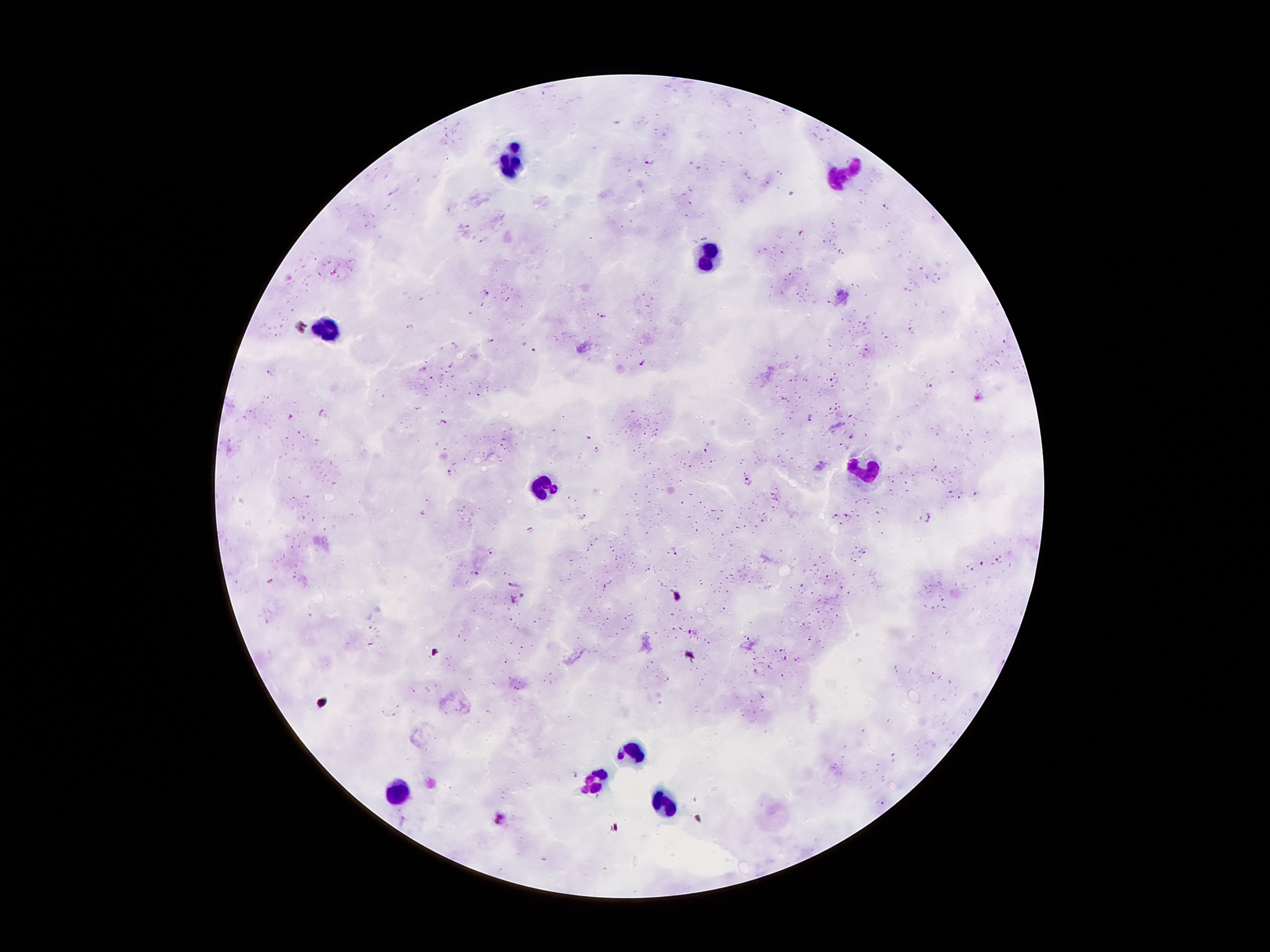

Approximate centers as [x, y] in pixels.
Summary:
  - Plasmodium parasite locations: [651, 159], [886, 208], [465, 228], [487, 293], [602, 316], [411, 326], [490, 341], [535, 350], [866, 352], [645, 363], [452, 365], [423, 369], [270, 372], [833, 381], [929, 386], [479, 394], [322, 414], [291, 416], [810, 417], [444, 422], [852, 436], [588, 437], [596, 450], [450, 473], [750, 481], [951, 493], [975, 495], [960, 497], [835, 515], [929, 516], [582, 517], [848, 517], [841, 524], [529, 530], [490, 551], [676, 551], [998, 559], [982, 564], [473, 574], [270, 580], [515, 585], [786, 658], [755, 671], [933, 673], [762, 697], [576, 774], [883, 803], [500, 818]
  - Leukocyte locations: [519, 142], [511, 168], [847, 176], [709, 258], [333, 327], [865, 469], [541, 485], [633, 749], [595, 781], [399, 795], [663, 801]
  - Preparation: thick peripheral-blood smear
  - Image size: 1270×952 pixels
  - Field of view: one from this slide
  - Capture: smartphone through the microscope eyepiece
  - Patient malaria status: infected with Plasmodium falciparum
  - Magnification: 100x
  - Stain: Giemsa